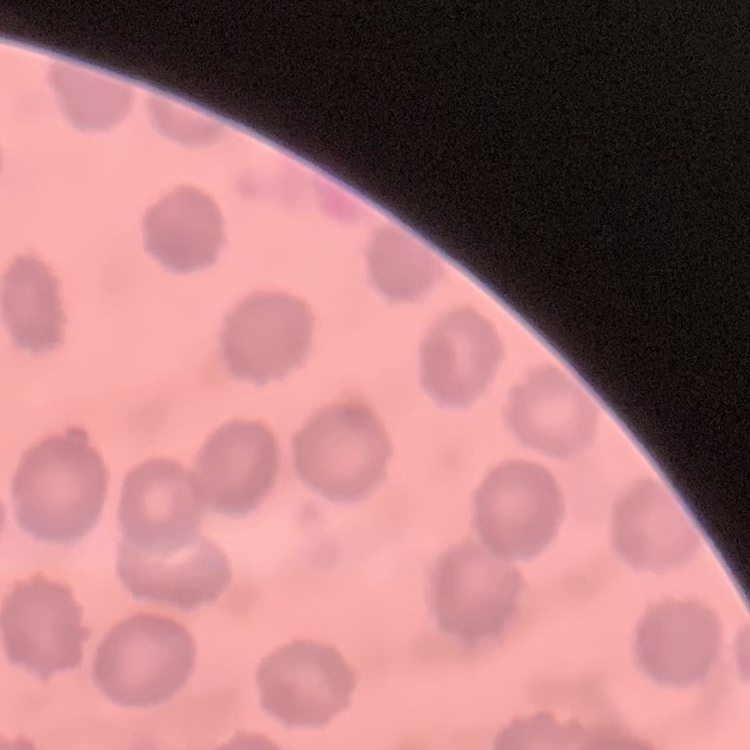

The erythrocytes exhibit no rouleaux formation. Square crop of a larger photomicrograph. Thin blood smear. Stained with either Field's or Giemsa.